Assess this cell for malaria.
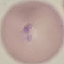
It is parasitized.

Giemsa-stained preparation. Acquired by smartphone through the microscope eyepiece. Automatically extracted cell patch, resized to 64 × 64 pixels. Thin smear of blood.